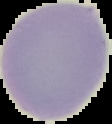

Summary:
  - Image size: 112×124 pixels
  - Result: negative for Plasmodium parasites
  - Image type: segmented cell region on a black background
  - Preparation: thin blood film